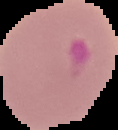
preparation = thin blood smear
malaria status = parasitized
image size = 118×130 pixels
image type = cell region segmented out of the field of view; surrounding area masked to black